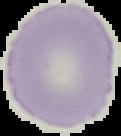 Image is 121×136 pixels. Cell region segmented out of the field of view; the surrounding area is masked to black. Malaria status: uninfected. From a thin blood smear.